State the blood parasite species.
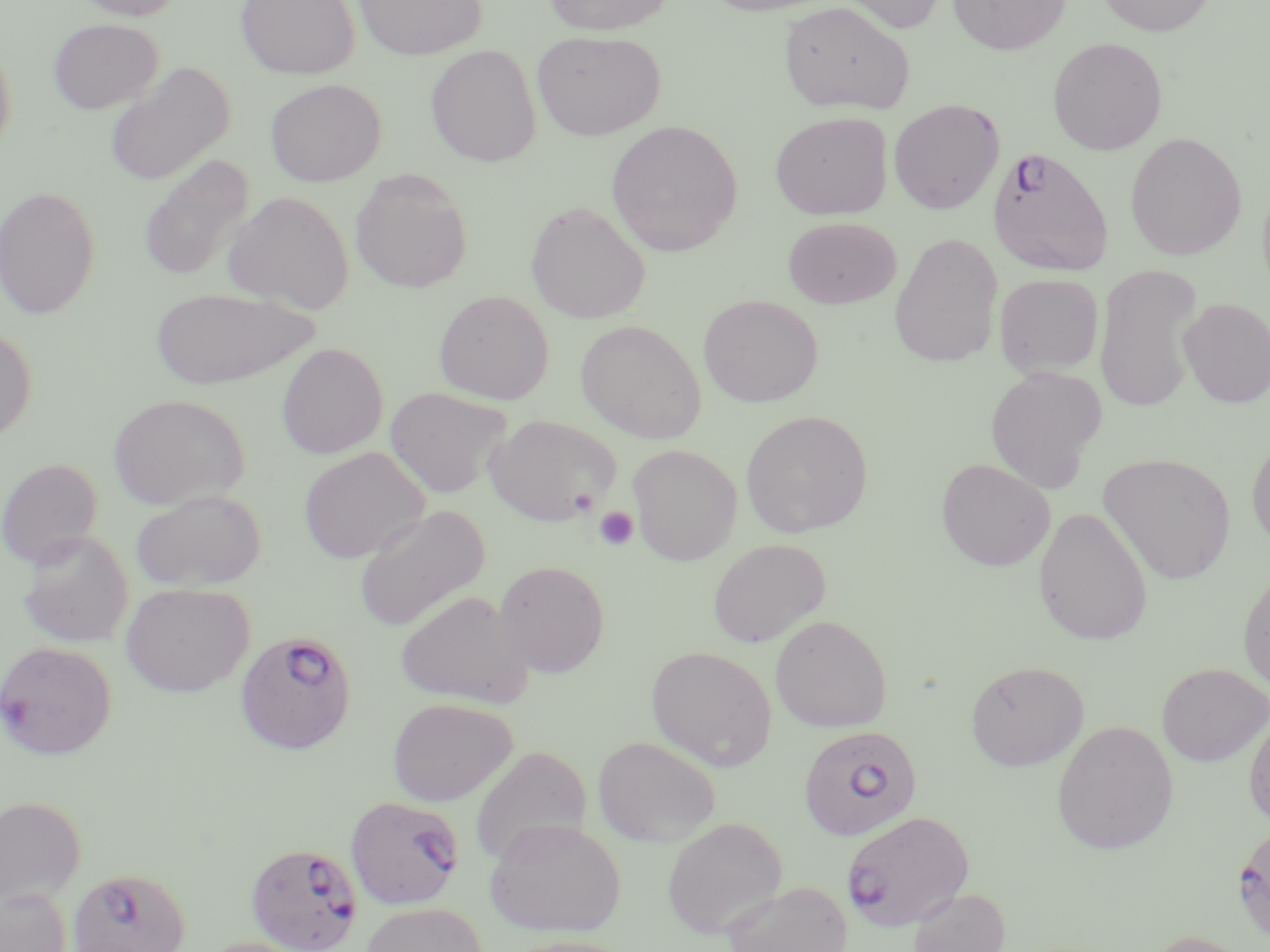

Plasmodium falciparum.

preparation = thin blood film
Plasmodium falciparum-infected red blood cell locations = approximate bounding boxes as (x1, y1, x2, y2) in pixels: (987, 146, 1114, 277), (234, 629, 356, 755), (798, 725, 922, 842), (345, 796, 464, 911), (841, 810, 974, 931), (1234, 822, 1270, 944), (245, 842, 362, 950), (69, 867, 190, 951)
modality = light microscopy
uninfected red blood cell locations = approximate bounding boxes as (x1, y1, x2, y2) in pixels: (69, 0, 190, 20), (235, 0, 360, 80), (353, 0, 487, 60), (541, 0, 676, 35), (702, 0, 842, 16), (832, 0, 952, 34), (948, 0, 1071, 55), (1095, 0, 1216, 36), (778, 1, 915, 116), (48, 18, 163, 114), (531, 30, 666, 141), (0, 34, 16, 157), (1047, 37, 1168, 155), (426, 45, 542, 167), (104, 62, 234, 187), (265, 78, 386, 186), (888, 99, 1005, 214), (770, 111, 893, 220), (605, 120, 743, 257), (1125, 132, 1247, 261), (138, 153, 254, 283), (349, 170, 473, 294), (0, 185, 101, 320), (223, 190, 355, 314), (525, 201, 651, 324), (783, 217, 901, 308), (889, 233, 1003, 368), (1094, 266, 1203, 413), (994, 274, 1104, 378), (150, 288, 318, 391), (433, 290, 554, 405), (699, 294, 823, 407), (1178, 297, 1270, 407), (576, 319, 706, 443), (0, 325, 36, 443), (276, 343, 388, 459), (985, 366, 1107, 494), (385, 387, 513, 499), (107, 393, 249, 510), (740, 410, 873, 538), (484, 415, 621, 526), (1247, 434, 1270, 554), (627, 443, 742, 565), (298, 446, 430, 563), (1097, 452, 1237, 584), (936, 457, 1055, 572), (0, 458, 103, 568), (130, 489, 266, 592), (355, 505, 490, 632), (1033, 507, 1153, 646), (17, 529, 133, 647), (708, 538, 831, 647), (493, 560, 611, 678), (1237, 569, 1270, 695), (121, 582, 254, 697), (395, 589, 534, 708), (770, 615, 892, 733), (0, 640, 117, 760), (646, 645, 778, 771), (965, 661, 1089, 771), (1157, 662, 1270, 766), (387, 697, 518, 806), (1244, 707, 1270, 830), (1051, 719, 1178, 855), (592, 736, 722, 847), (469, 745, 592, 867), (0, 795, 87, 908), (662, 816, 788, 940), (484, 818, 626, 937), (722, 880, 853, 952), (0, 886, 71, 952), (908, 887, 1011, 952), (360, 902, 488, 952), (1142, 929, 1259, 952), (500, 936, 634, 952), (196, 937, 318, 952)
magnification = 1000x
platelet locations = approximate bounding boxes as (x1, y1, x2, y2) in pixels: (570, 487, 599, 516), (593, 506, 639, 551)
stain = May-Grünwald-Giemsa
image size = 1270×952 pixels
field of view = single